Assess this cell for malaria.
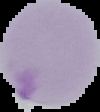
It is parasitized.

Summary:
  - Image size: 100×112 pixels
  - Preparation: thin blood film
  - Image type: segmented cell region with the area outside set to black